Locate every blood parasite and identify its species.
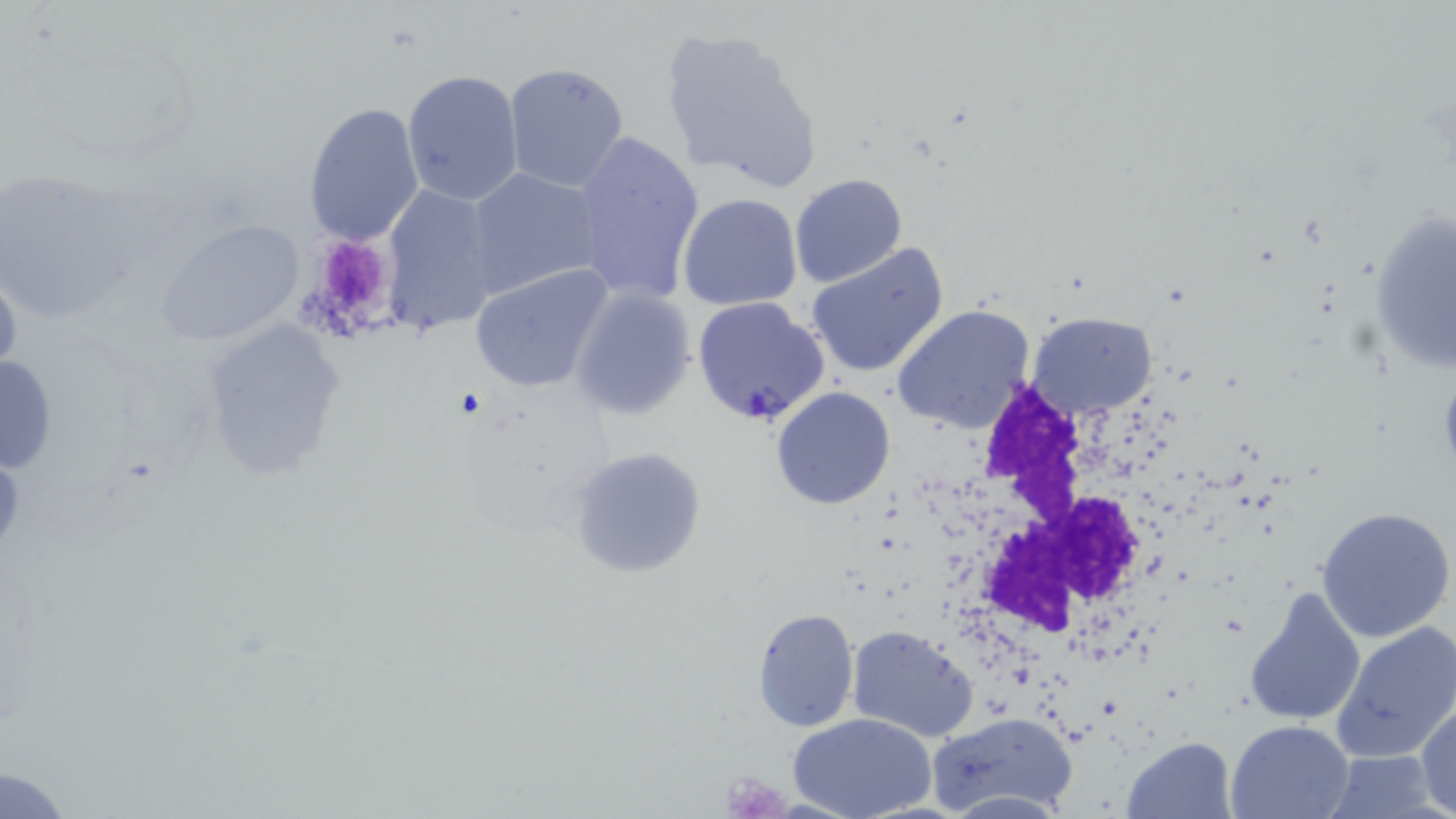

Approximate bounding boxes as [x1, y1, x2, y2] in pixels.
Plasmodium falciparum-infected red blood cells: [691, 295, 830, 426].
No Plasmodium ovale, Plasmodium malariae, Plasmodium vivax, Babesia divergens, or Trypanosoma brucei observed.

slide_level_diagnosis: Plasmodium falciparum
platelet_locations: 'approximate bounding boxes as [x1, y1, x2, y2] in pixels: [299, 233, 401, 340], [721, 772, 788, 815]'
field_of_view: single
stain: May-Grünwald-Giemsa
image_size: 1456×819 pixels
uninfected_red_blood_cell_locations: 'approximate bounding boxes as [x1, y1, x2, y2] in pixels: [658, 27, 821, 194], [502, 61, 632, 193], [402, 71, 526, 209], [301, 100, 427, 247], [569, 131, 705, 306], [467, 166, 605, 298], [0, 171, 139, 329], [789, 173, 907, 289], [381, 181, 504, 335], [678, 193, 802, 311], [1369, 206, 1454, 380], [154, 217, 307, 346], [806, 243, 949, 378], [0, 257, 22, 389], [467, 264, 614, 394], [568, 284, 697, 421], [892, 306, 1034, 432], [1028, 312, 1156, 419], [199, 316, 348, 481], [0, 354, 58, 479], [770, 387, 896, 510], [566, 445, 705, 580], [1315, 506, 1454, 642], [1243, 585, 1367, 728], [751, 607, 859, 732], [1332, 621, 1456, 765], [847, 625, 980, 744], [1415, 700, 1456, 816], [931, 711, 1078, 819], [791, 713, 936, 819], [1227, 719, 1354, 818], [1123, 736, 1235, 818], [1324, 751, 1441, 818], [1, 766, 76, 819]'
white_blood_cell_locations: 'approximate bounding boxes as [x1, y1, x2, y2] in pixels: [972, 381, 1171, 668]'
magnification: 1000x
modality: light microscopy
preparation: thin blood smear